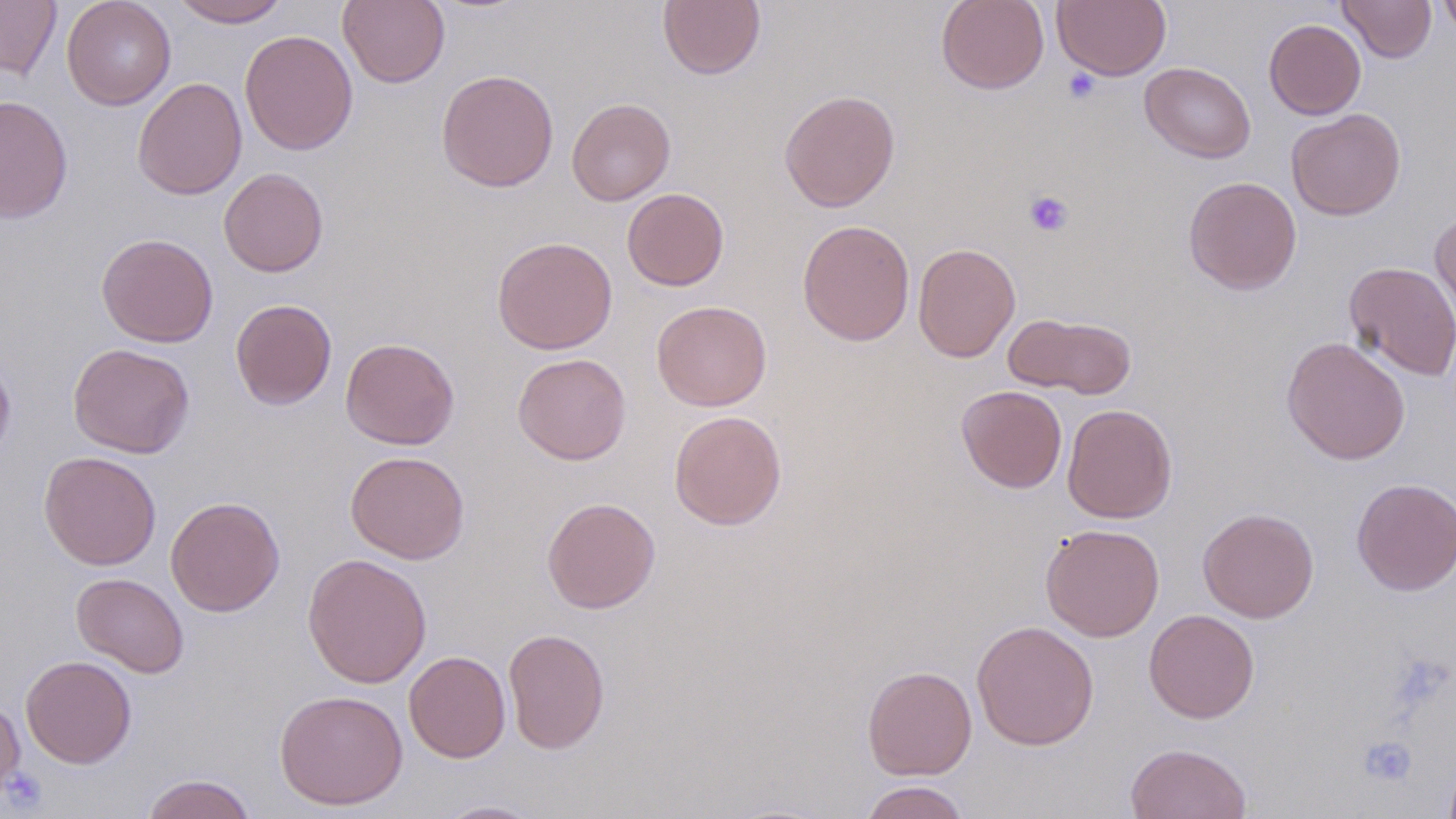

slide-level diagnosis = negative for blood parasites
image size = 1456×819 pixels
uninfected red blood cell locations = approximate bounding boxes as named x1/y1/x2/y2 corners in pixels: (x1=0, y1=0, x2=62, y2=80), (x1=61, y1=0, x2=177, y2=110), (x1=170, y1=0, x2=290, y2=28), (x1=338, y1=0, x2=450, y2=88), (x1=658, y1=0, x2=765, y2=80), (x1=936, y1=0, x2=1049, y2=94), (x1=1052, y1=0, x2=1171, y2=81), (x1=1338, y1=0, x2=1436, y2=63), (x1=1436, y1=0, x2=1456, y2=39), (x1=1264, y1=19, x2=1366, y2=120), (x1=240, y1=29, x2=358, y2=155), (x1=1140, y1=62, x2=1256, y2=163), (x1=436, y1=68, x2=559, y2=192), (x1=132, y1=77, x2=247, y2=200), (x1=779, y1=89, x2=901, y2=212), (x1=0, y1=95, x2=74, y2=222), (x1=567, y1=97, x2=675, y2=205), (x1=1286, y1=108, x2=1406, y2=221), (x1=219, y1=167, x2=329, y2=277), (x1=1183, y1=176, x2=1302, y2=294), (x1=622, y1=188, x2=729, y2=291), (x1=1429, y1=209, x2=1456, y2=330), (x1=797, y1=219, x2=915, y2=346), (x1=96, y1=232, x2=218, y2=347), (x1=492, y1=236, x2=618, y2=355), (x1=913, y1=242, x2=1021, y2=363), (x1=1344, y1=261, x2=1456, y2=382), (x1=230, y1=298, x2=337, y2=410), (x1=651, y1=300, x2=772, y2=411), (x1=1005, y1=313, x2=1138, y2=399), (x1=1281, y1=336, x2=1411, y2=465), (x1=340, y1=337, x2=460, y2=450), (x1=67, y1=342, x2=195, y2=459), (x1=0, y1=350, x2=16, y2=466), (x1=512, y1=353, x2=631, y2=464), (x1=956, y1=385, x2=1067, y2=493), (x1=1062, y1=403, x2=1178, y2=524), (x1=668, y1=410, x2=787, y2=531), (x1=39, y1=451, x2=161, y2=571), (x1=345, y1=451, x2=470, y2=564), (x1=1351, y1=478, x2=1456, y2=595), (x1=165, y1=496, x2=285, y2=616), (x1=541, y1=496, x2=661, y2=614), (x1=1197, y1=507, x2=1320, y2=623), (x1=1040, y1=523, x2=1165, y2=642), (x1=302, y1=552, x2=432, y2=689), (x1=71, y1=572, x2=189, y2=677), (x1=1143, y1=608, x2=1260, y2=723), (x1=971, y1=619, x2=1099, y2=750), (x1=503, y1=628, x2=610, y2=754), (x1=403, y1=650, x2=511, y2=763), (x1=20, y1=655, x2=137, y2=768), (x1=862, y1=665, x2=977, y2=780), (x1=274, y1=689, x2=409, y2=811), (x1=0, y1=696, x2=26, y2=801), (x1=1124, y1=742, x2=1252, y2=819), (x1=141, y1=773, x2=257, y2=819), (x1=859, y1=780, x2=970, y2=819), (x1=434, y1=800, x2=547, y2=818)
magnification = 1000x
field of view = one of a larger specimen
stain = May-Grünwald-Giemsa
modality = optical microscopy
platelet locations = approximate bounding boxes as named x1/y1/x2/y2 corners in pixels: (x1=1063, y1=69, x2=1101, y2=103), (x1=1024, y1=190, x2=1074, y2=237), (x1=1360, y1=735, x2=1417, y2=786), (x1=2, y1=767, x2=48, y2=814)
preparation = thin blood film